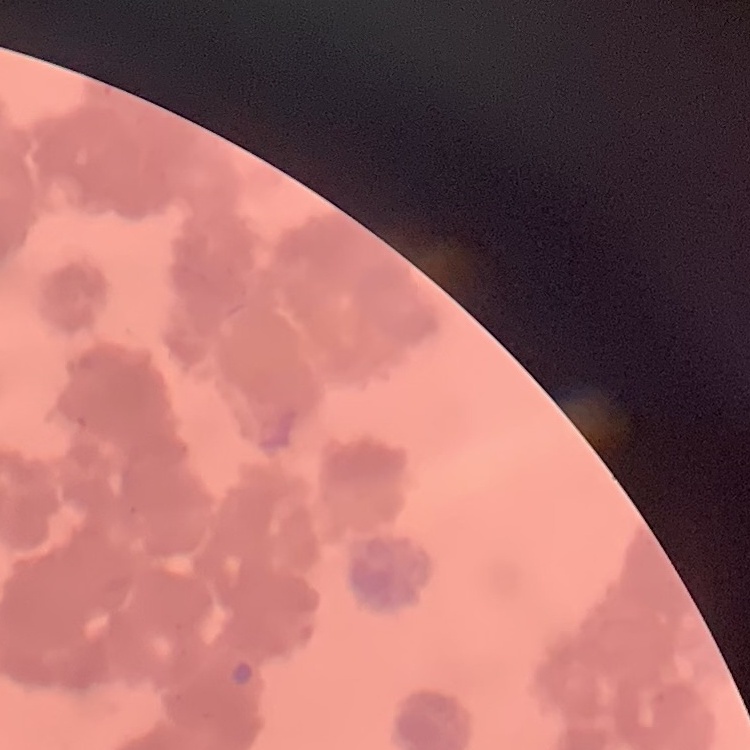

{
  "erythrocyte_morphology": "rouleaux formation",
  "image_type": "square crop of a larger photomicrograph",
  "stain": "Field's or Giemsa",
  "preparation": "thin peripheral smear"
}